Classify this cell by malaria status.
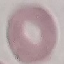

Uninfected.

Summary:
  - Capture: smartphone through the microscope eyepiece
  - Preparation: thin smear
  - Image type: cell patch, automatically extracted from a larger field of view and resized to 64 × 64 pixels
  - Stain: Giemsa